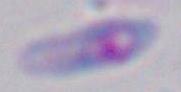
Summary:
  - Magnification: 1000x
  - Modality: micrograph
  - Identification: Toxoplasma gondii